Identify the cell.
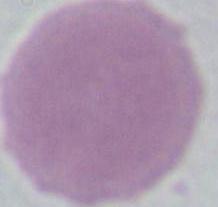

An erythrocyte.

magnification = 1000x
modality = photomicrograph